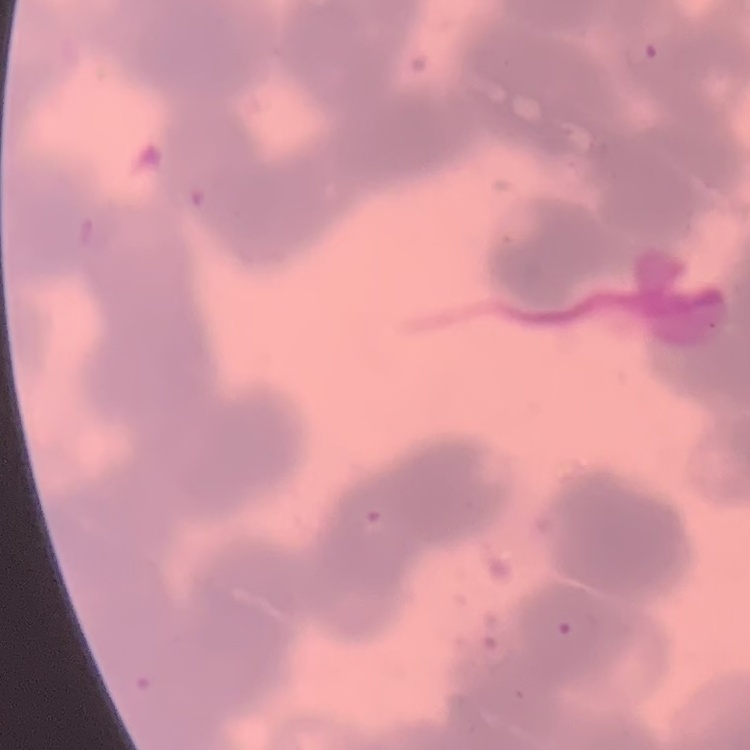
red blood cell morphology = rouleaux formation
preparation = thin blood smear
image type = one tile cut from a larger photomicrograph
stain = Field's or Giemsa